Classify this cell by malaria status.
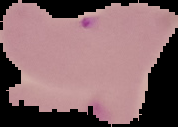
It is parasitized.

Summary:
  - Image size: 178×127 pixels
  - Preparation: thin blood film
  - Image type: segmented cell region with the area outside set to black